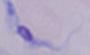

Summary:
  - Magnification: 1000x
  - Identification: trypanosome
  - Modality: photomicrograph